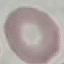

Malaria status: uninfected. Automatically extracted cell patch, resized to 64 × 64 pixels. Thin smear of blood. Giemsa-stained preparation. Photographed with a smartphone camera at the microscope eyepiece.